State which parasite is depicted.
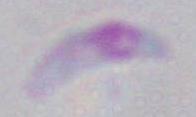

Toxoplasma gondii.

Summary:
  - Magnification: 1000x
  - Modality: micrograph